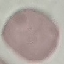

Result: no malaria parasites seen. Thin blood film. Acquired by smartphone through the microscope eyepiece. Cell patch, automatically extracted from a larger field of view and resized to 64 × 64 pixels. Giemsa-stained preparation.